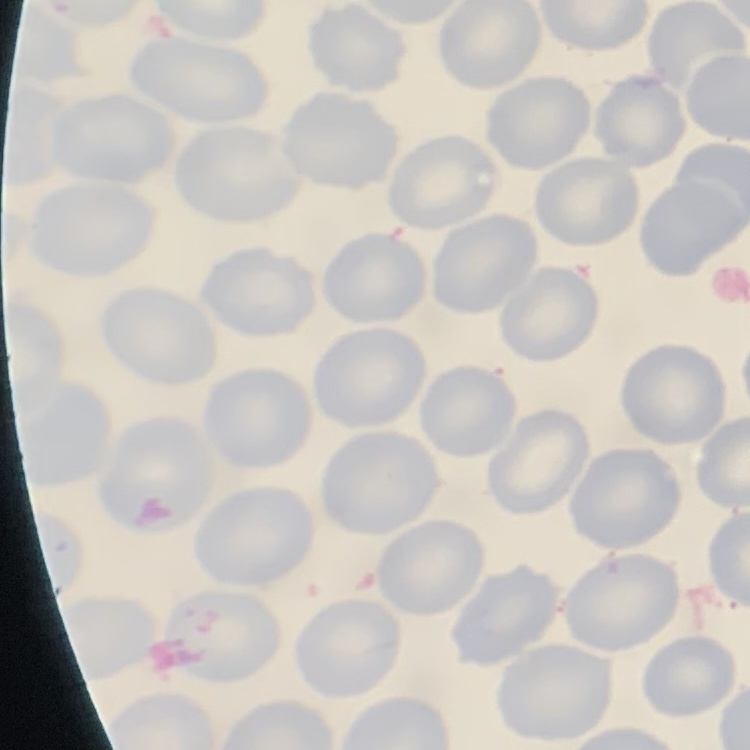

The red blood cells show no rouleaux formation. Thin peripheral smear. One tile cut from a larger photomicrograph. Field's or Giemsa stain.